Classify this cell by malaria status.
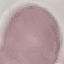
It is uninfected.

Photographed with a smartphone camera at the microscope eyepiece. Thin blood film. Automatically extracted cell patch, resized to 64 × 64 pixels. Giemsa stain.